Report the malaria status of this cell.
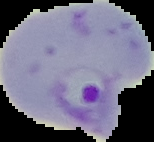

It is parasitized.

The area outside the segmented cell region is set to black. From a thin blood film. Image is 154×142 pixels.